Assess this cell for malaria.
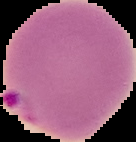
It is parasitized.

The area outside the segmented cell region is set to black. Image is 136×142 pixels. From a thin blood film.